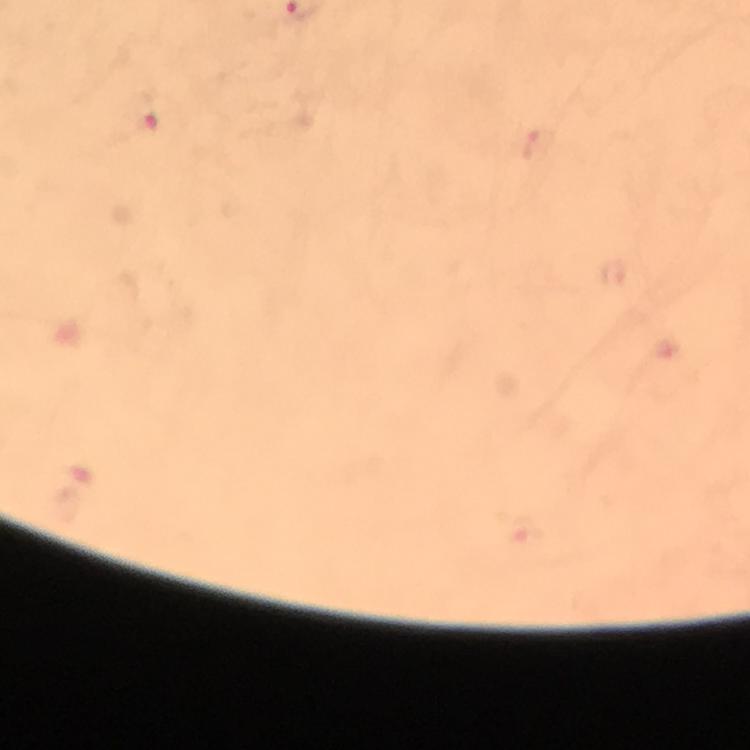
Approximate centers as [x, y] in pixels.
Summary:
  - Plasmodium parasite locations: [144, 119]
  - Capture: smartphone mounted on the microscope
  - Context: from a diagnostic examination for malaria
  - Immersion oil: used
  - Cropped from: a single field of view
  - Image size: 750×750 pixels
  - Preparation: thick smear
  - Magnification: 100x
  - Stain: Giemsa